Assess this cell for malaria.
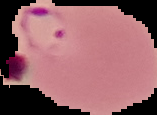
Parasitized.

{
  "preparation": "thin blood smear",
  "image_size": "157×115 pixels",
  "image_type": "cell region segmented out of the field of view; surrounding area masked to black"
}